Give the position of every leukocyte visible.
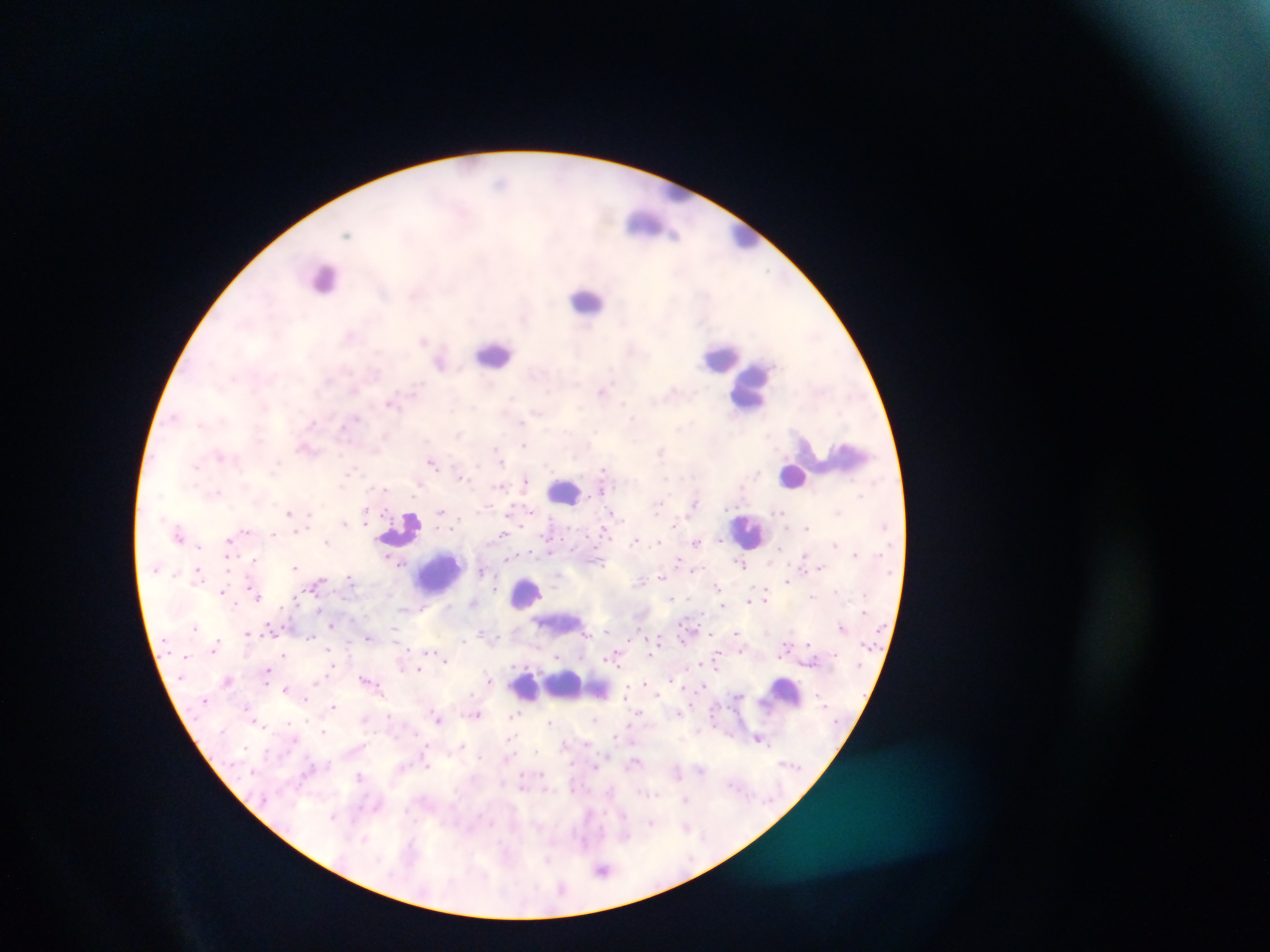
Approximate centers as {x, y} in pixels.
Leukocytes: {679, 193}, {649, 224}, {745, 235}, {324, 278}, {587, 300}, {495, 353}, {722, 357}, {751, 386}, {845, 457}, {793, 475}, {563, 491}, {401, 528}, {750, 531}, {440, 574}, {527, 595}, {570, 687}, {528, 689}, {784, 693}.

Plasmodium parasite locations: {424, 342}, {441, 362}, {603, 392}, {313, 422}, {307, 447}, {433, 462}, {461, 476}, {526, 480}, {601, 489}, {694, 503}, {290, 511}, {441, 511}, {614, 512}, {345, 522}, {365, 522}, {806, 527}, {520, 528}, {605, 531}, {246, 532}, {273, 534}, {503, 534}, {179, 535}, {636, 539}, {229, 540}, {327, 540}, {697, 542}, {199, 546}, {551, 551}, {855, 551}, {805, 554}, {228, 556}, {508, 557}, {257, 559}, {679, 560}, {401, 562}, {741, 564}, {296, 566}, {822, 567}, {694, 569}, {198, 570}, {481, 571}, {661, 575}, {351, 578}, {788, 580}, {642, 581}, {318, 582}, {250, 584}, {718, 588}, {495, 589}, {223, 592}, {256, 595}, {813, 595}, {671, 597}, {767, 597}, {750, 598}, {297, 600}, {474, 602}, {724, 606}, {282, 607}, {448, 607}, {331, 625}, {196, 628}, {842, 628}, {606, 630}, {735, 631}, {247, 632}, {711, 634}, {310, 636}, {370, 637}, {216, 642}, {807, 644}, {214, 648}, {741, 650}, {426, 653}, {283, 654}, {560, 654}, {650, 654}, {614, 656}, {445, 659}, {703, 662}, {718, 665}, {418, 670}, {267, 671}, {227, 680}, {488, 680}, {269, 681}, {647, 683}, {703, 685}, {287, 688}, {628, 689}, {305, 699}, {333, 706}, {639, 711}, {678, 712}, {477, 713}, {512, 715}, {439, 719}, {255, 720}, {551, 722}, {323, 733}, {759, 738}, {565, 744}, {596, 766}, {360, 776}, {521, 788}, {545, 788}, {687, 799}, {652, 822}, {686, 825}, {602, 869}. Image is 1270×952 pixels. Mobile-phone photograph taken through the microscope. One field of view. Collected in Ghana. Thick blood film.